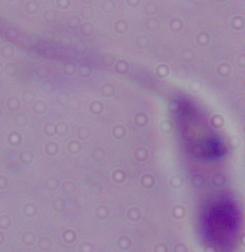

Summary:
  - Modality: micrograph
  - Magnification: 1000x
  - Identification: Leishmania